Name the blood parasite species.
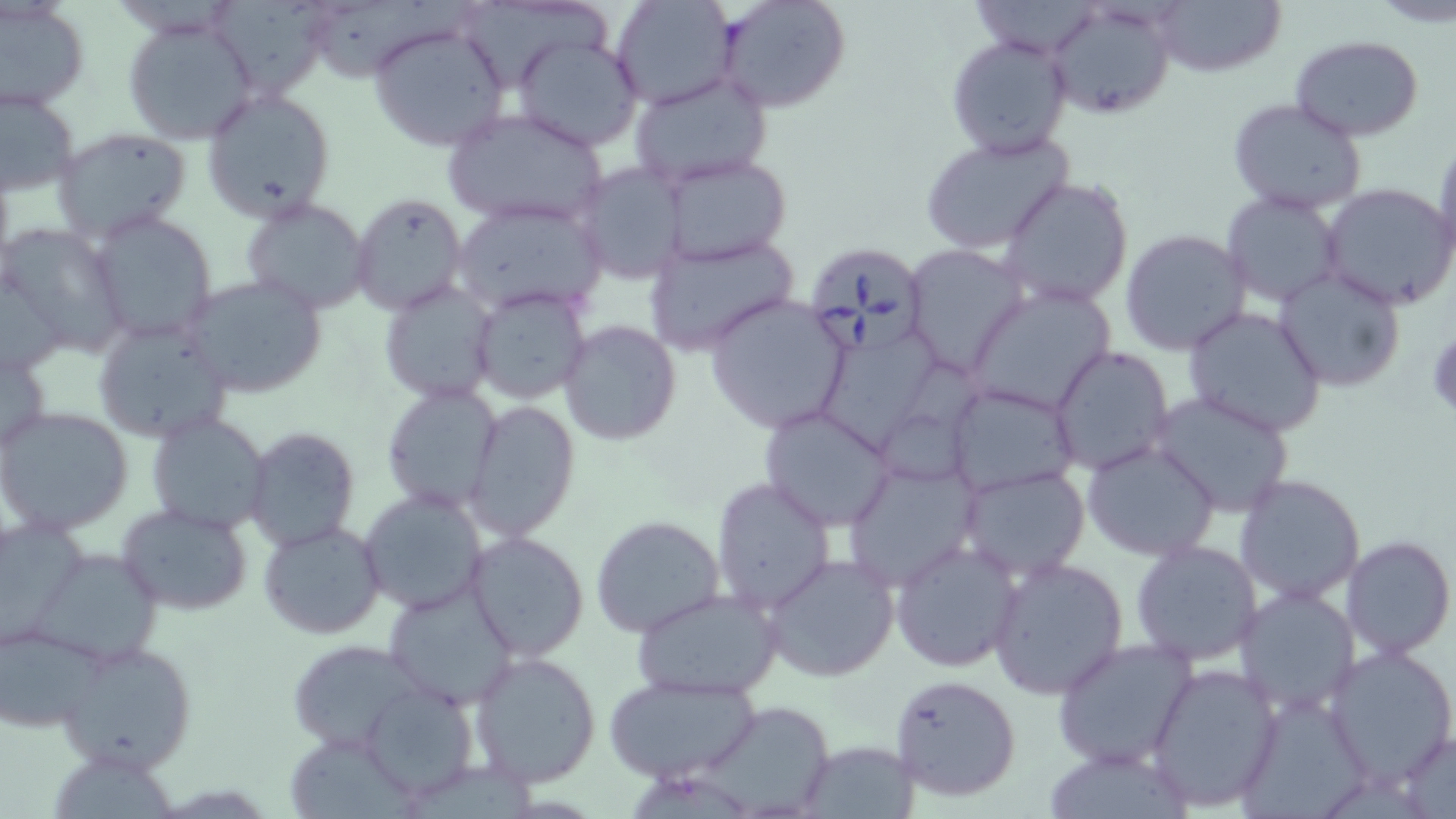
Babesia divergens.

Approximate bounding boxes as named x1/y1/x2/y2 corners in pixels. Babesia divergens-infected red blood cell locations: (x1=802, y1=241, x2=932, y2=358). Uninfected red blood cell locations: (x1=212, y1=0, x2=330, y2=101), (x1=611, y1=0, x2=737, y2=109), (x1=716, y1=0, x2=852, y2=113), (x1=972, y1=0, x2=1101, y2=57), (x1=1152, y1=0, x2=1286, y2=79), (x1=1049, y1=1, x2=1175, y2=120), (x1=1, y1=2, x2=90, y2=110), (x1=316, y1=2, x2=473, y2=84), (x1=469, y1=5, x2=612, y2=91), (x1=119, y1=13, x2=262, y2=146), (x1=368, y1=23, x2=510, y2=153), (x1=511, y1=34, x2=644, y2=153), (x1=946, y1=34, x2=1072, y2=157), (x1=1290, y1=35, x2=1426, y2=141), (x1=627, y1=72, x2=774, y2=190), (x1=2, y1=86, x2=81, y2=196), (x1=201, y1=88, x2=337, y2=222), (x1=1226, y1=96, x2=1370, y2=217), (x1=444, y1=108, x2=609, y2=228), (x1=52, y1=127, x2=194, y2=243), (x1=918, y1=131, x2=1073, y2=253), (x1=1432, y1=139, x2=1456, y2=269), (x1=660, y1=154, x2=793, y2=264), (x1=573, y1=162, x2=688, y2=284), (x1=998, y1=175, x2=1135, y2=308), (x1=1319, y1=182, x2=1456, y2=309), (x1=1220, y1=189, x2=1346, y2=310), (x1=351, y1=194, x2=466, y2=313), (x1=241, y1=198, x2=371, y2=315), (x1=452, y1=201, x2=606, y2=316), (x1=86, y1=209, x2=218, y2=344), (x1=0, y1=224, x2=127, y2=356), (x1=1120, y1=228, x2=1251, y2=356), (x1=645, y1=231, x2=799, y2=356), (x1=903, y1=244, x2=1029, y2=375), (x1=0, y1=263, x2=70, y2=381), (x1=1274, y1=267, x2=1406, y2=392), (x1=184, y1=275, x2=327, y2=398), (x1=378, y1=280, x2=500, y2=405), (x1=967, y1=282, x2=1118, y2=418), (x1=472, y1=285, x2=593, y2=405), (x1=703, y1=294, x2=851, y2=434), (x1=1182, y1=307, x2=1327, y2=437), (x1=93, y1=317, x2=235, y2=445), (x1=558, y1=320, x2=682, y2=446), (x1=820, y1=333, x2=942, y2=457), (x1=1, y1=345, x2=53, y2=458), (x1=1050, y1=345, x2=1174, y2=475), (x1=883, y1=361, x2=1001, y2=481), (x1=945, y1=382, x2=1079, y2=496), (x1=382, y1=384, x2=505, y2=515), (x1=1149, y1=390, x2=1297, y2=518), (x1=464, y1=398, x2=581, y2=542), (x1=1, y1=406, x2=134, y2=535), (x1=760, y1=406, x2=897, y2=532), (x1=146, y1=411, x2=271, y2=534), (x1=245, y1=426, x2=360, y2=551), (x1=1083, y1=440, x2=1220, y2=561), (x1=843, y1=460, x2=980, y2=592), (x1=959, y1=466, x2=1089, y2=581), (x1=1235, y1=474, x2=1367, y2=606), (x1=712, y1=476, x2=836, y2=613), (x1=359, y1=486, x2=489, y2=615), (x1=116, y1=503, x2=256, y2=617), (x1=0, y1=515, x2=90, y2=643), (x1=590, y1=516, x2=727, y2=639), (x1=257, y1=521, x2=387, y2=641), (x1=466, y1=531, x2=592, y2=663), (x1=1341, y1=535, x2=1455, y2=659), (x1=891, y1=538, x2=1025, y2=672), (x1=1130, y1=540, x2=1263, y2=667), (x1=33, y1=548, x2=164, y2=667), (x1=761, y1=554, x2=901, y2=682), (x1=986, y1=558, x2=1128, y2=699), (x1=383, y1=580, x2=520, y2=707), (x1=630, y1=588, x2=782, y2=701), (x1=1234, y1=588, x2=1360, y2=716), (x1=2, y1=620, x2=107, y2=733), (x1=287, y1=638, x2=424, y2=751), (x1=1051, y1=638, x2=1197, y2=770), (x1=55, y1=640, x2=198, y2=775), (x1=1325, y1=644, x2=1456, y2=784), (x1=469, y1=650, x2=603, y2=789), (x1=1145, y1=661, x2=1285, y2=812), (x1=889, y1=673, x2=1023, y2=803), (x1=603, y1=674, x2=761, y2=783), (x1=361, y1=683, x2=480, y2=802), (x1=1242, y1=695, x2=1372, y2=819), (x1=701, y1=708, x2=835, y2=816), (x1=1396, y1=730, x2=1456, y2=815), (x1=799, y1=739, x2=920, y2=817), (x1=290, y1=741, x2=416, y2=817), (x1=1039, y1=744, x2=1195, y2=816), (x1=62, y1=757, x2=179, y2=819). One field of a larger specimen. Light microscopy. Image is 1456×819 pixels. Thin blood film. 1000x magnification. May-Grünwald-Giemsa stain.